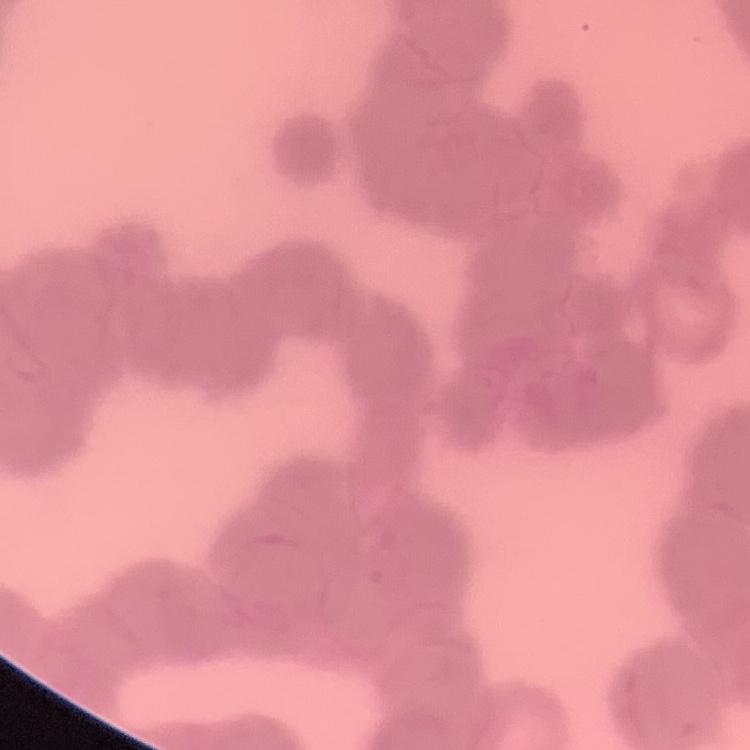
erythrocyte morphology = rouleaux formation
preparation = thin peripheral smear
stain = Field's or Giemsa
image type = one tile cut from a larger photomicrograph